Report the malaria status of this cell.
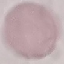

It is uninfected.

Summary:
  - Capture: smartphone camera at the microscope eyepiece
  - Stain: Giemsa
  - Preparation: thin blood film
  - Image type: automatically extracted cell patch, resized to 64 × 64 pixels